Assess this cell for malaria.
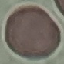

Uninfected.

Summary:
  - Preparation: thin smear
  - Capture: smartphone camera at the microscope eyepiece
  - Stain: Giemsa
  - Image type: automatically extracted cell patch, resized to 64 × 64 pixels